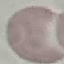

Malaria status: uninfected. Photographed with a smartphone camera at the microscope eyepiece. Giemsa stain. Automatically extracted cell patch, resized to 64 × 64 pixels. Thin blood film.